Give the position of every malaria parasite.
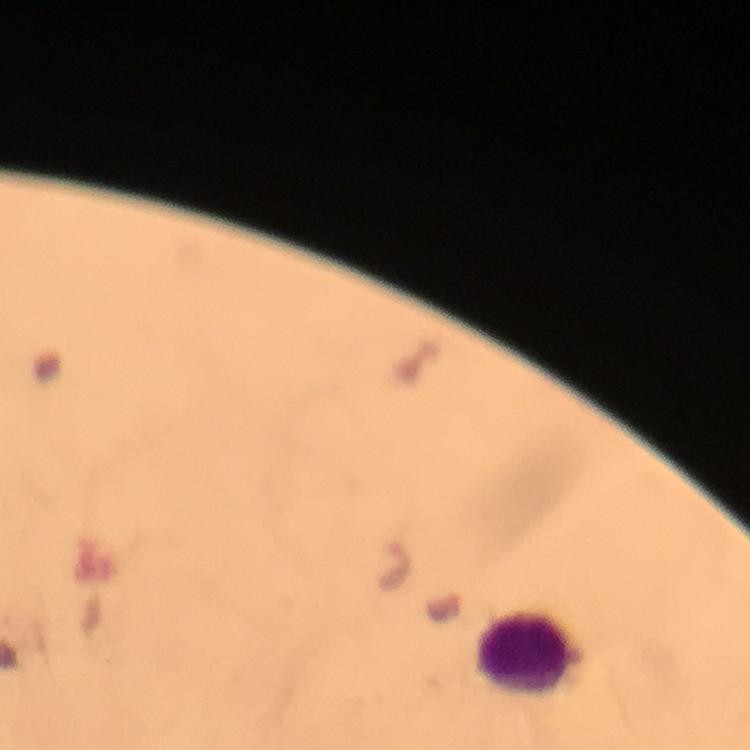
Approximate centers as {x, y} in pixels.
Malaria parasites: {398, 569}.

cropped_from: a single field of view
magnification: 100x
stain: Giemsa
image_size: 750×750 pixels
context: from a malaria diagnostic workup
preparation: thick blood film
capture: smartphone photograph through a microscope
leukocyte_locations: 'approximate centers as {x, y} in pixels: {522, 652}'
immersion_oil: used